Name the parasite shown.
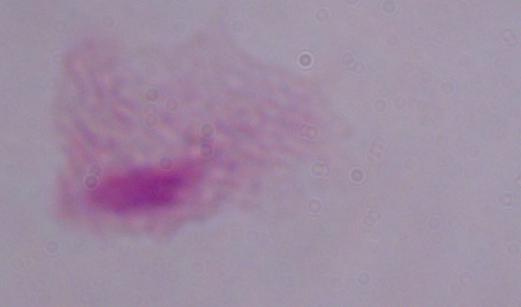
A trichomonad.

Photomicrograph. Captured at 1000x magnification.